Outline each blood parasite and name the species.
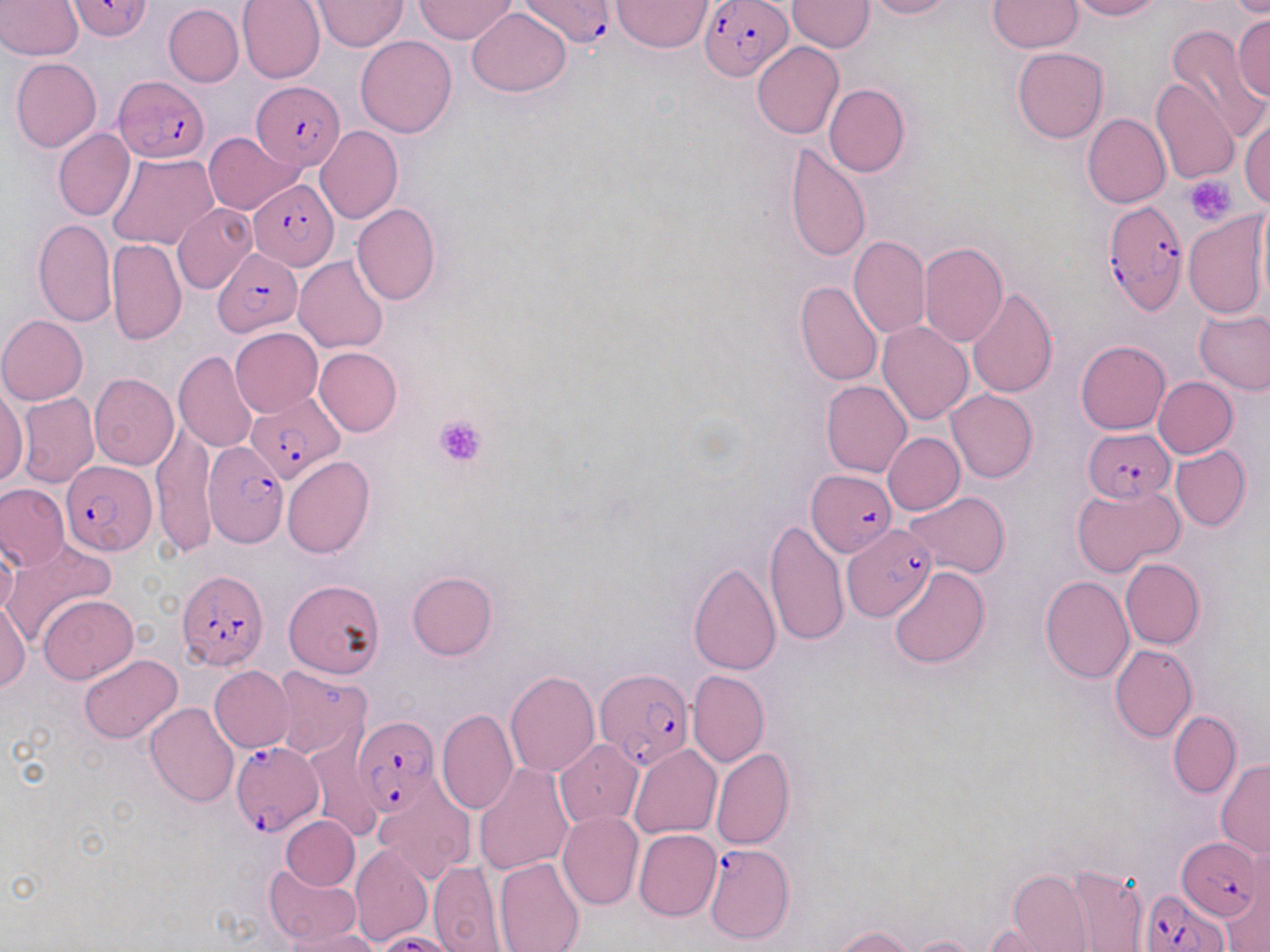
Approximate bounding boxes as [x1, y1, x2, y2] in pixels.
Plasmodium falciparum-infected red blood cells: [66, 0, 153, 42], [518, 0, 613, 50], [700, 1, 792, 79], [117, 77, 209, 161], [253, 82, 345, 169], [248, 180, 339, 271], [1101, 201, 1188, 315], [212, 248, 302, 336], [247, 393, 344, 483], [1084, 426, 1174, 504], [204, 436, 290, 553], [60, 459, 157, 555], [807, 469, 895, 557], [842, 523, 937, 623], [176, 570, 271, 672], [594, 668, 695, 774], [352, 717, 440, 818], [231, 741, 323, 835], [1177, 836, 1260, 919], [704, 845, 792, 944], [1139, 887, 1230, 952].
No Plasmodium ovale, Plasmodium malariae, Plasmodium vivax, Babesia divergens, or Trypanosoma brucei observed.

Uninfected red blood cell locations: [0, 0, 82, 59], [413, 0, 516, 43], [613, 0, 712, 52], [864, 0, 954, 19], [1067, 0, 1163, 21], [1221, 0, 1270, 17], [237, 1, 325, 84], [311, 1, 409, 50], [789, 1, 873, 52], [987, 1, 1083, 52], [163, 3, 244, 87], [467, 7, 571, 97], [1234, 13, 1269, 101], [1165, 25, 1268, 143], [354, 35, 457, 137], [752, 42, 844, 139], [1012, 47, 1108, 143], [10, 58, 102, 152], [1151, 76, 1241, 186], [823, 83, 909, 178], [1240, 108, 1270, 210], [1083, 113, 1171, 208], [315, 126, 402, 224], [53, 129, 134, 220], [203, 132, 303, 215], [784, 143, 871, 263], [109, 153, 220, 251], [1254, 200, 1269, 309], [171, 203, 258, 294], [351, 203, 441, 304], [1183, 210, 1268, 318], [34, 220, 116, 327], [848, 235, 929, 339], [107, 239, 186, 345], [918, 242, 1008, 346], [294, 256, 390, 355], [794, 281, 883, 386], [965, 287, 1058, 399], [1194, 311, 1270, 394], [0, 315, 88, 405], [877, 321, 973, 425], [229, 327, 322, 417], [1076, 340, 1170, 434], [313, 347, 403, 437], [173, 351, 258, 453], [89, 373, 178, 470], [1153, 376, 1237, 458], [821, 380, 911, 478], [1, 385, 29, 484], [946, 389, 1038, 482], [16, 393, 99, 489], [151, 426, 218, 557], [883, 432, 965, 515], [1170, 445, 1250, 531], [282, 456, 375, 558], [0, 484, 67, 570], [1073, 485, 1181, 578], [903, 491, 1010, 579], [764, 517, 848, 646], [0, 539, 21, 624], [3, 541, 114, 648], [1120, 558, 1204, 649], [688, 562, 781, 675], [890, 566, 990, 669], [406, 572, 497, 660], [1040, 576, 1134, 683], [284, 580, 385, 678], [38, 593, 139, 684], [0, 600, 30, 692], [1110, 643, 1197, 742], [78, 654, 183, 744], [271, 665, 372, 760], [209, 666, 293, 752], [687, 669, 769, 767], [505, 670, 599, 777], [146, 702, 240, 807], [436, 709, 519, 816], [1168, 710, 1241, 798], [301, 732, 385, 842], [554, 739, 643, 828], [629, 743, 723, 838], [711, 749, 794, 849], [1216, 758, 1270, 857], [474, 762, 573, 874], [372, 780, 476, 884], [557, 810, 642, 909], [281, 815, 360, 890], [635, 828, 722, 921], [350, 843, 433, 946], [493, 856, 585, 952], [428, 859, 504, 952], [1065, 864, 1149, 950], [265, 866, 360, 947], [1005, 869, 1093, 951], [1220, 881, 1269, 950], [984, 921, 1061, 952], [834, 926, 918, 952], [282, 929, 380, 952], [908, 936, 984, 952]. Platelet locations: [1185, 174, 1235, 225], [433, 412, 489, 468]. Slide-level diagnosis: Plasmodium falciparum. Single field of view. May-Grünwald-Giemsa-stained preparation. Light microscopy. Thin blood film. Image is 1270×952 pixels. 1000x magnification.